Classify this cell by malaria status.
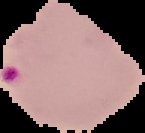

Parasitized.

Summary:
  - Image type: segmented cell region on a black background
  - Image size: 145×133 pixels
  - Preparation: thin blood film